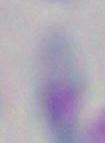
Toxoplasma gondii is shown. Photomicrograph. Captured at 1000x magnification.